Name the parasite shown.
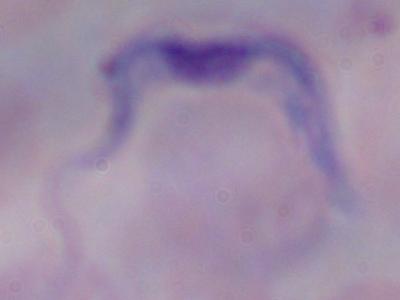
A trypanosome.

Summary:
  - Magnification: 1000x
  - Modality: photomicrograph